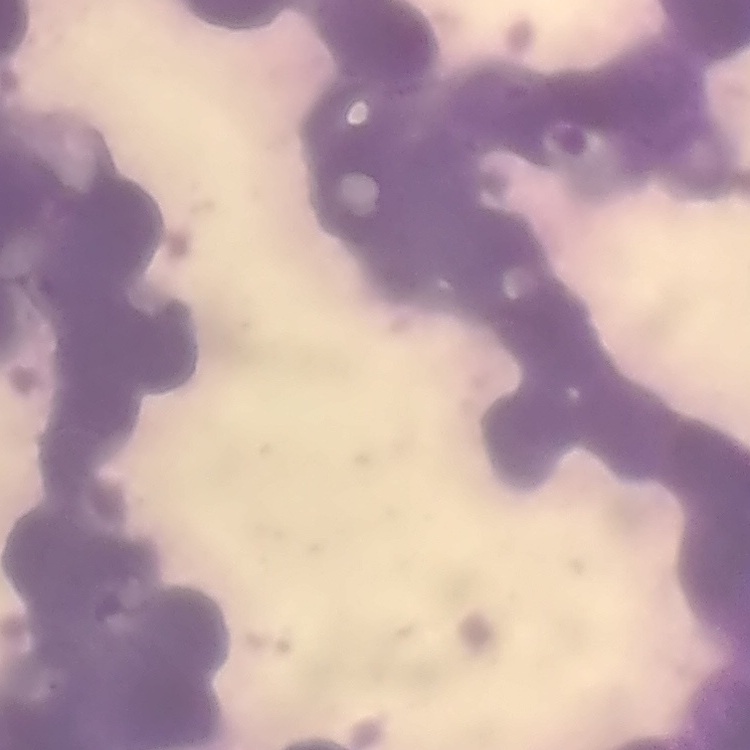

The red blood cells exhibit rouleaux formation. Field's or Giemsa stain. Thin blood film. Square crop of a larger photomicrograph.